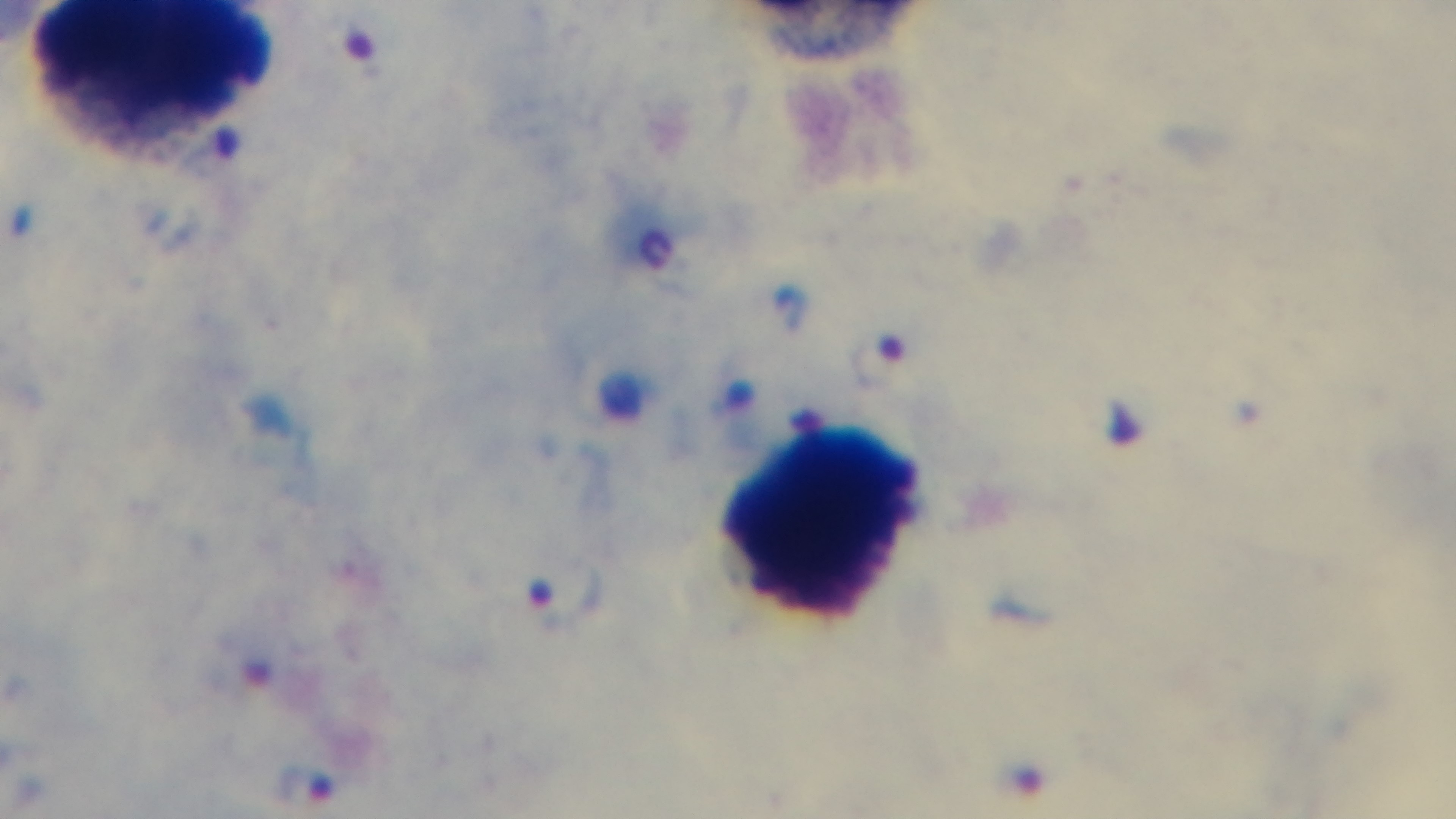

Mounted 4K digital camera. Photomicrograph. Malaria status: positive. 100x oil-immersion objective. Giemsa stain. Preparation: thick smear. One field from the slide.